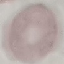

Malaria status: uninfected. Automatically extracted cell patch, resized to 64 × 64 pixels. Giemsa-stained preparation. Acquired by smartphone through the microscope eyepiece. Thin smear of blood.